Assess this cell for malaria.
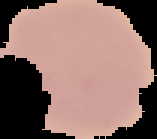
It is uninfected.

preparation = thin blood film
image size = 157×139 pixels
image type = segmented cell region with the area outside set to black